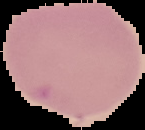

Summary:
  - Result: no Plasmodium parasites seen
  - Preparation: thin blood smear
  - Image type: segmented cell region with the area outside set to black
  - Image size: 145×130 pixels